Report the malaria status of this cell.
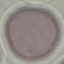

It is uninfected.

Acquired by smartphone through the microscope eyepiece. Cell patch, automatically extracted from a larger field of view and resized to 64 × 64 pixels. Giemsa stain. Thin blood smear.